Assess this cell for malaria.
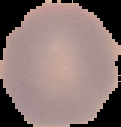

It is uninfected.

Cell region segmented out of the field of view; the surrounding area is masked to black. From a thin blood film. Image is 121×127 pixels.